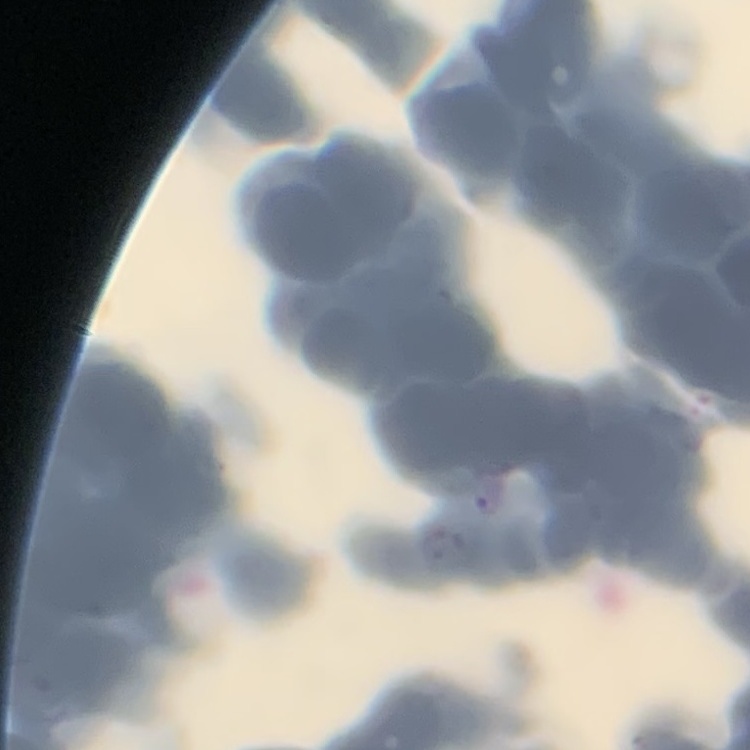

The red blood cells exhibit rouleaux formation. Field's or Giemsa stain. Thin blood film. Square crop of a larger photomicrograph.